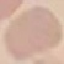

Summary:
  - Malaria status: uninfected
  - Preparation: thin blood film
  - Capture: smartphone through the microscope eyepiece
  - Stain: Giemsa
  - Image type: automatically extracted cell patch, resized to 64 × 64 pixels